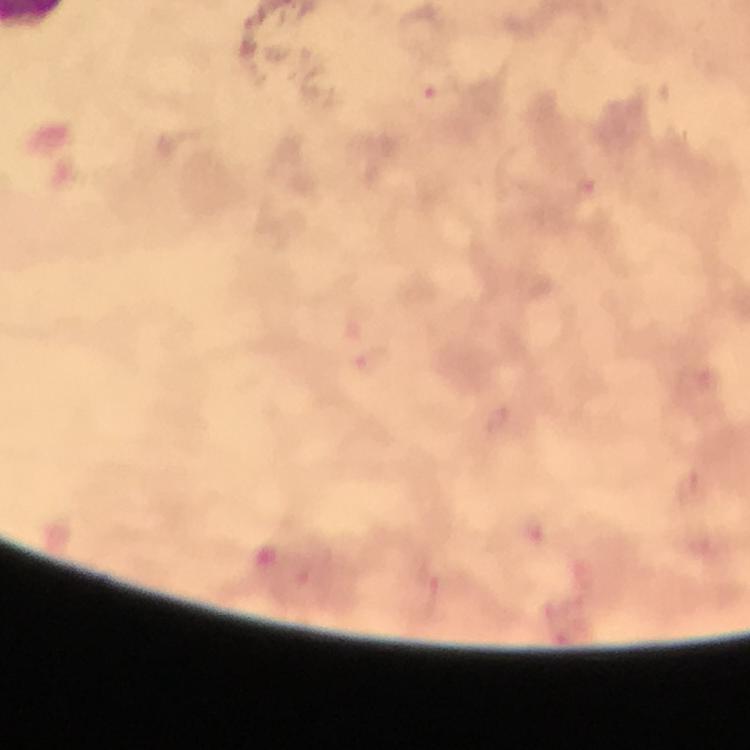
Approximate object centers, in pixels from the top-left corner. Plasmodium parasite locations: (x=430, y=89), (x=586, y=189), (x=371, y=359), (x=433, y=597). From a diagnostic examination for malaria. Photographed through the microscope with a smartphone camera. At 100x magnification. Immersion oil was used. Cropped region of a single field of view. Image is 750×750 pixels. Thick blood film. Giemsa stain.